Classify this cell by malaria status.
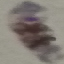
It is parasitized.

Acquired by smartphone through the microscope eyepiece. Thin smear of blood. Cell patch, automatically extracted from a larger field of view and resized to 64 × 64 pixels. Giemsa-stained preparation.